State which parasite is depicted.
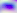

Toxoplasma gondii.

400x magnification. Micrograph.